Locate every Plasmodium ovale-infected red blood cell.
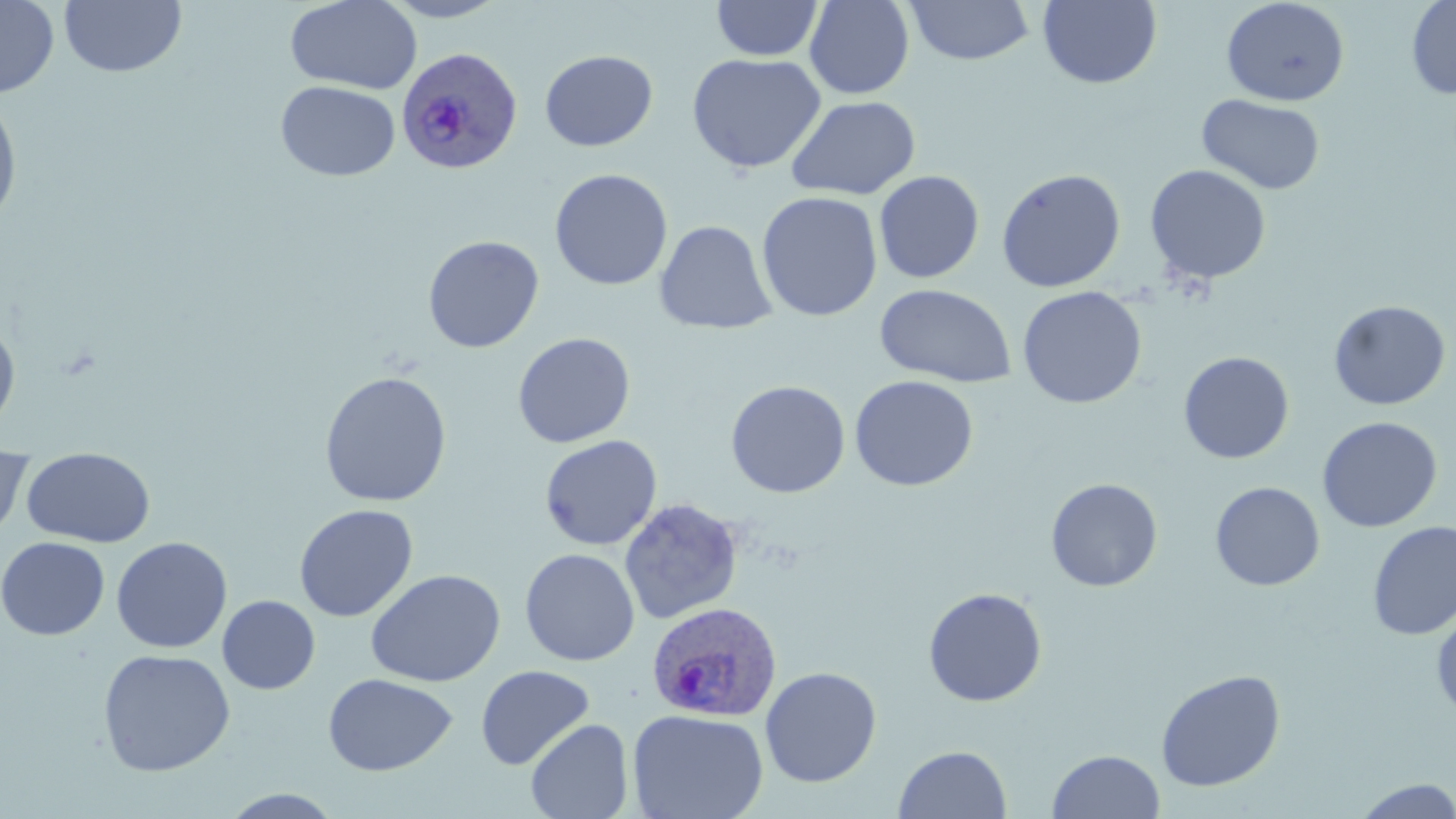
Approximate bounding boxes as [x1, y1, x2, y2] in pixels.
Plasmodium ovale-infected red blood cells: [396, 46, 523, 175], [646, 601, 782, 722].

Uninfected red blood cell locations: [0, 0, 59, 99], [285, 0, 422, 94], [379, 0, 509, 22], [804, 0, 914, 99], [1220, 0, 1350, 106], [1406, 0, 1456, 100], [59, 1, 187, 78], [711, 1, 824, 61], [905, 1, 1035, 66], [1037, 1, 1162, 89], [539, 49, 658, 151], [687, 53, 825, 174], [276, 80, 400, 181], [0, 90, 24, 230], [1197, 94, 1326, 195], [786, 95, 921, 201], [1144, 164, 1271, 285], [550, 168, 673, 291], [996, 168, 1126, 293], [873, 170, 985, 284], [756, 191, 883, 322], [655, 220, 777, 335], [422, 235, 544, 354], [874, 283, 1016, 388], [1017, 286, 1147, 409], [1328, 300, 1451, 410], [0, 317, 21, 435], [512, 332, 636, 448], [1178, 351, 1294, 464], [319, 371, 453, 507], [849, 375, 978, 491], [725, 380, 851, 498], [1317, 416, 1442, 533], [539, 434, 663, 551], [21, 449, 156, 548], [0, 450, 33, 541], [1045, 478, 1163, 592], [1210, 481, 1325, 591], [618, 498, 744, 625], [294, 503, 418, 622], [1367, 520, 1456, 640], [111, 536, 232, 653], [0, 537, 110, 640], [519, 548, 640, 666], [365, 569, 505, 687], [923, 587, 1047, 707], [217, 595, 320, 694], [1432, 607, 1456, 722], [97, 648, 235, 777], [476, 664, 595, 770], [760, 666, 883, 788], [1155, 669, 1286, 792], [323, 672, 457, 776], [627, 708, 769, 819], [525, 718, 634, 819], [893, 744, 1012, 819], [1047, 749, 1165, 819], [1352, 778, 1456, 818], [219, 789, 347, 818]. Slide-level diagnosis: Plasmodium ovale. Image is 1456×819 pixels. Single field of view. Optical microscopy. 1000x magnification. Thin blood smear. May-Grünwald-Giemsa stain.